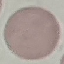

Summary:
  - Result: no malaria parasites detected
  - Preparation: thin blood film
  - Capture: smartphone through the microscope eyepiece
  - Stain: Giemsa
  - Image type: cell patch, automatically extracted from a larger field of view and resized to 64 × 64 pixels